Assess the morphology of the red blood cells.
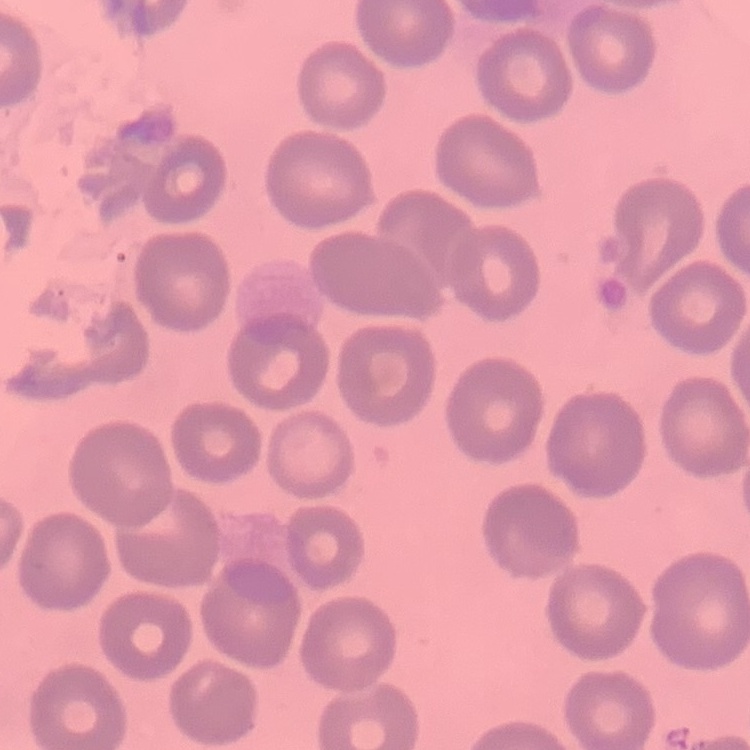

They show no rouleaux formation.

Summary:
  - Preparation: thin peripheral smear
  - Stain: Field's or Giemsa
  - Image type: one tile cut from a larger photomicrograph